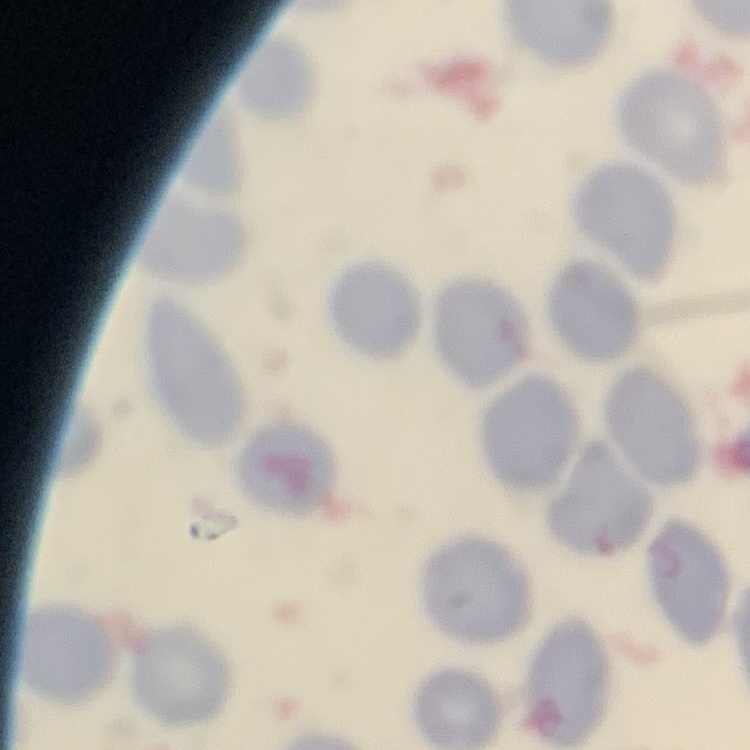
Summary:
  - Red blood cell morphology: no rouleaux formation
  - Stain: Field's or Giemsa
  - Preparation: thin blood film
  - Image type: square crop of a larger photomicrograph